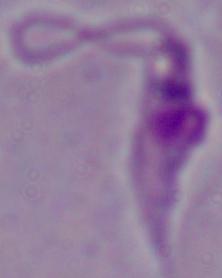

{
  "modality": "photomicrograph",
  "identification": "Leishmania",
  "magnification": "1000x"
}